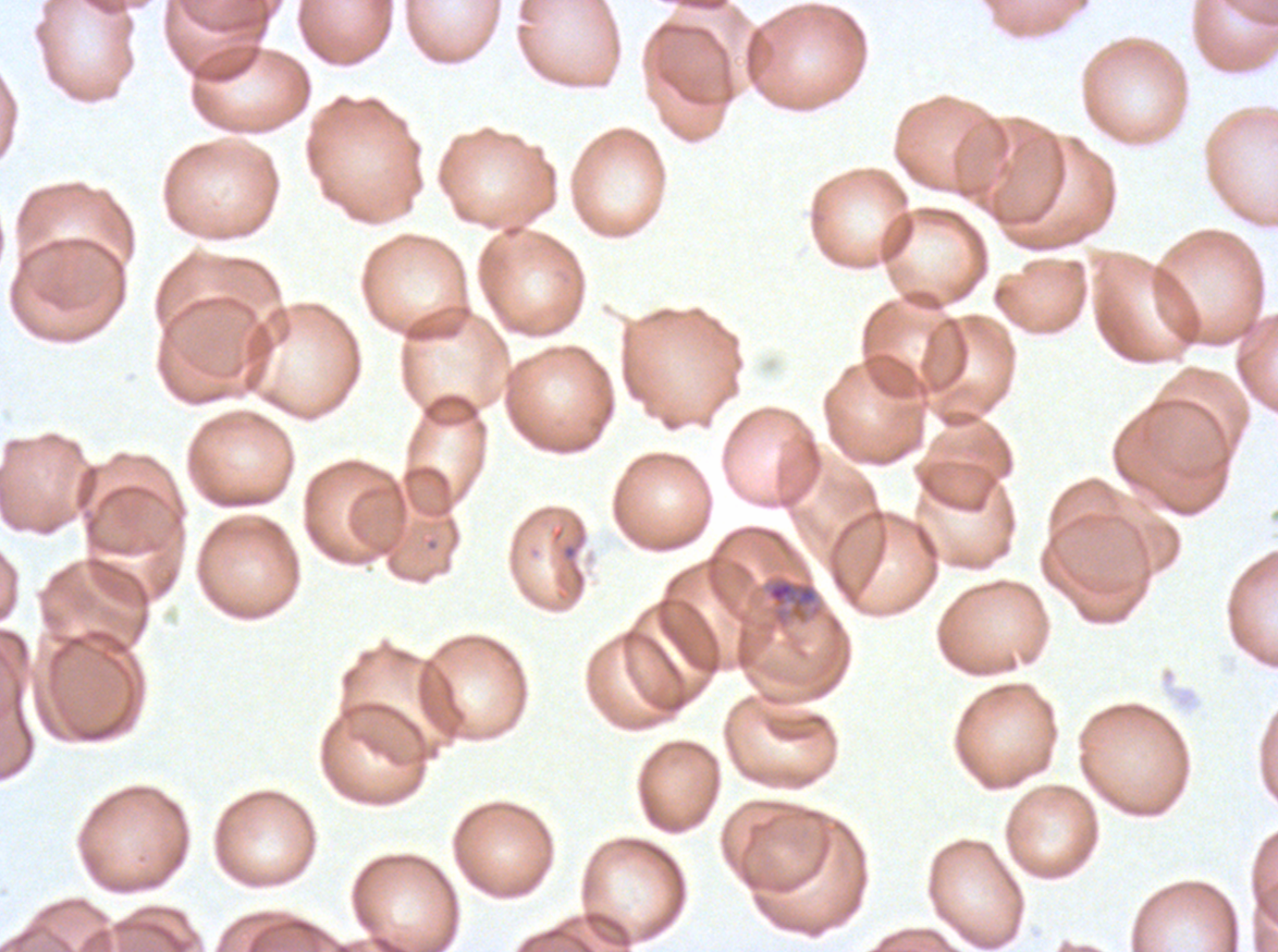 Approximate bounding boxes as (x1, y1, x2, y2) in pixels. Late-ring/early-trophozoite locations: (766, 577, 818, 624). Image is 1278×952 pixels. P. falciparum from a patient in The Gambia, cultured ex vivo for 24 to 48 hours. Thin blood smear. Giemsa-stained preparation. A sub-image separated from a larger composite.